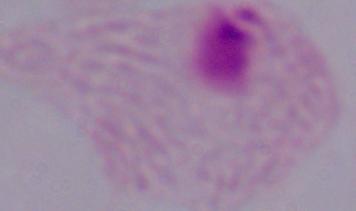 Captured at 1000x magnification. Micrograph. A trichomonad is shown.